Locate every Plasmodium parasite.
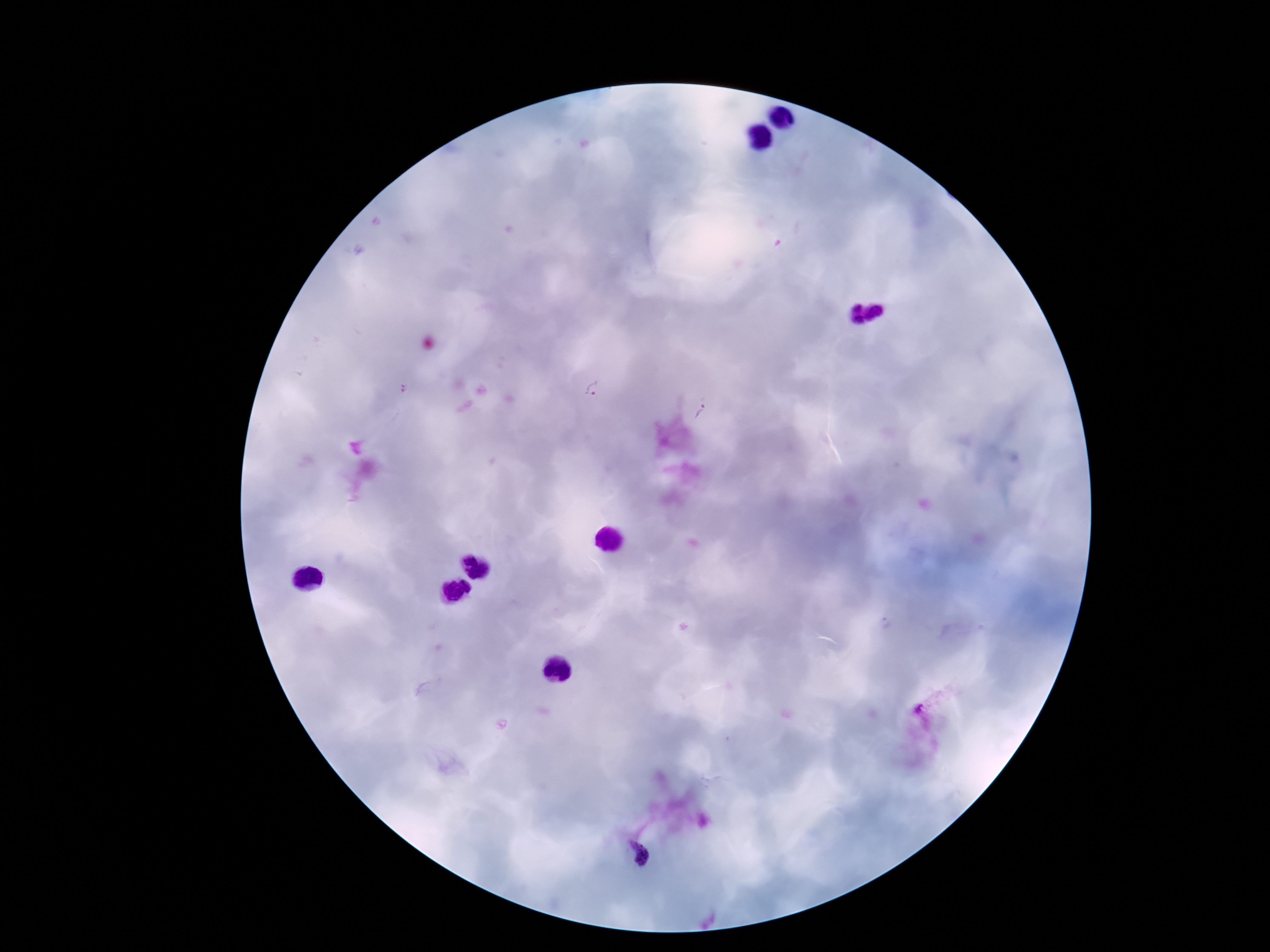
Approximate object centers, in pixels from the top-left corner.
Plasmodium parasites: (x=593, y=389), (x=704, y=410), (x=639, y=854).

Smartphone photograph taken through the microscope eyepiece. Single field of view. Giemsa stain. 100x magnification. Thick blood film. Image is 1270×952 pixels. Patient malaria status: positive.